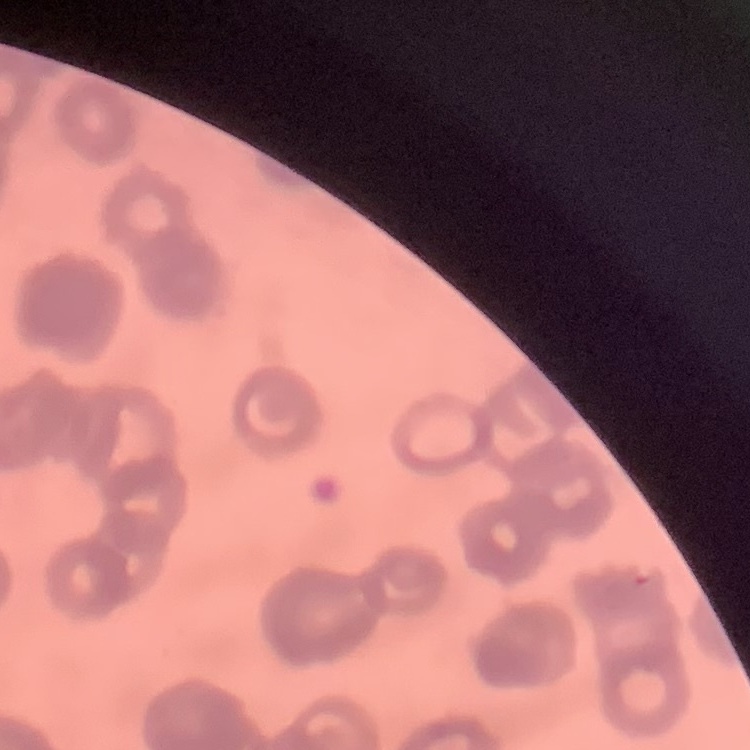
red_blood_cell_morphology: rouleaux formation
preparation: thin blood smear
stain: Field's or Giemsa
image_type: one tile cut from a larger photomicrograph